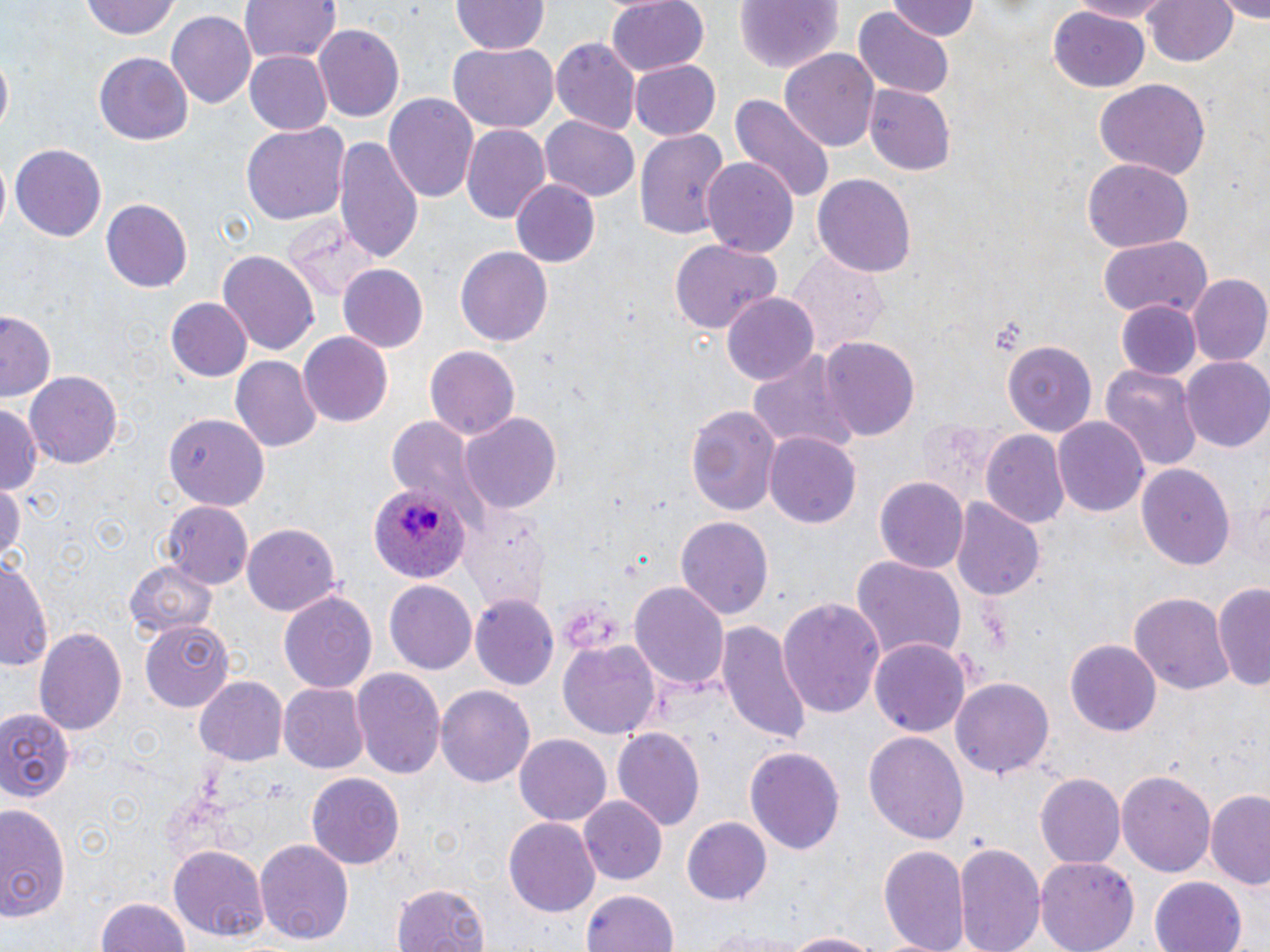

Summary:
  - Coordinate format: approximate bounding boxes as (x1, y1, x2, y2) in pixels
  - Uninfected red blood cell locations: (240, 0, 340, 67), (607, 0, 710, 74), (1063, 0, 1174, 22), (1143, 0, 1239, 69), (1218, 0, 1270, 21), (80, 1, 182, 42), (451, 1, 548, 57), (734, 1, 844, 74), (887, 1, 981, 43), (1050, 6, 1151, 92), (856, 8, 954, 96), (167, 11, 257, 111), (313, 24, 405, 123), (551, 39, 641, 134), (446, 43, 558, 133), (781, 47, 880, 153), (244, 51, 332, 135), (94, 53, 193, 146), (0, 56, 12, 133), (630, 60, 721, 140), (1093, 78, 1211, 180), (866, 85, 956, 175), (383, 92, 479, 203), (728, 92, 836, 207), (539, 116, 641, 201), (241, 122, 350, 226), (460, 124, 549, 221), (637, 126, 730, 244), (333, 136, 423, 263), (10, 143, 108, 242), (1083, 156, 1192, 251), (702, 159, 798, 256), (813, 172, 915, 277), (510, 180, 600, 266), (101, 198, 193, 291), (285, 218, 380, 302), (1096, 235, 1212, 320), (668, 238, 782, 335), (454, 245, 553, 349), (217, 251, 319, 355), (787, 252, 890, 358), (339, 265, 429, 353), (1187, 275, 1270, 367), (724, 293, 818, 385), (168, 297, 251, 382), (1117, 301, 1199, 379), (1, 309, 59, 403), (297, 331, 393, 427), (820, 336, 918, 442), (1003, 339, 1100, 434), (424, 346, 520, 442), (746, 349, 856, 454), (232, 357, 322, 454), (1182, 358, 1270, 454), (1100, 364, 1203, 472), (26, 371, 122, 470), (0, 401, 42, 496), (685, 402, 782, 516), (460, 412, 561, 513), (165, 414, 268, 509), (386, 415, 490, 526), (1053, 416, 1149, 516), (980, 430, 1070, 529), (766, 432, 861, 528), (1138, 461, 1235, 573), (0, 478, 25, 565), (875, 478, 968, 572), (951, 498, 1043, 602), (165, 500, 252, 590), (466, 509, 548, 611), (675, 516, 773, 620), (241, 523, 342, 617), (850, 553, 967, 665), (0, 557, 52, 674), (126, 559, 216, 639), (630, 579, 729, 691), (386, 580, 477, 675), (1216, 583, 1270, 693), (279, 589, 378, 695), (1132, 590, 1233, 697), (471, 595, 560, 692), (778, 597, 885, 721), (717, 619, 813, 748), (138, 620, 235, 711), (35, 626, 127, 734), (867, 637, 971, 738), (559, 638, 659, 741), (1067, 639, 1160, 737), (352, 669, 445, 782), (196, 677, 288, 764), (951, 678, 1055, 779), (279, 683, 368, 774), (436, 685, 534, 789), (0, 706, 75, 804), (611, 726, 704, 830), (863, 731, 969, 847), (515, 732, 611, 825), (745, 745, 846, 855), (1118, 770, 1216, 880), (306, 771, 405, 868), (1037, 775, 1124, 868), (1206, 791, 1270, 888), (580, 796, 668, 885), (0, 803, 71, 924), (681, 815, 773, 905), (504, 818, 599, 917), (255, 840, 355, 945), (953, 840, 1045, 952), (881, 841, 970, 952), (170, 845, 269, 940), (1036, 856, 1138, 952), (1149, 876, 1249, 952), (392, 882, 492, 952), (579, 889, 681, 952), (96, 898, 193, 951), (703, 926, 811, 950), (779, 931, 889, 952)
  - Plasmodium ovale-infected red blood cell locations: (368, 482, 473, 586)
  - Slide-level diagnosis: Plasmodium ovale
  - Field of view: single
  - Preparation: thin blood smear
  - Stain: May-Grünwald-Giemsa
  - Modality: light microscopy
  - Magnification: 1000x
  - Image size: 1270×952 pixels